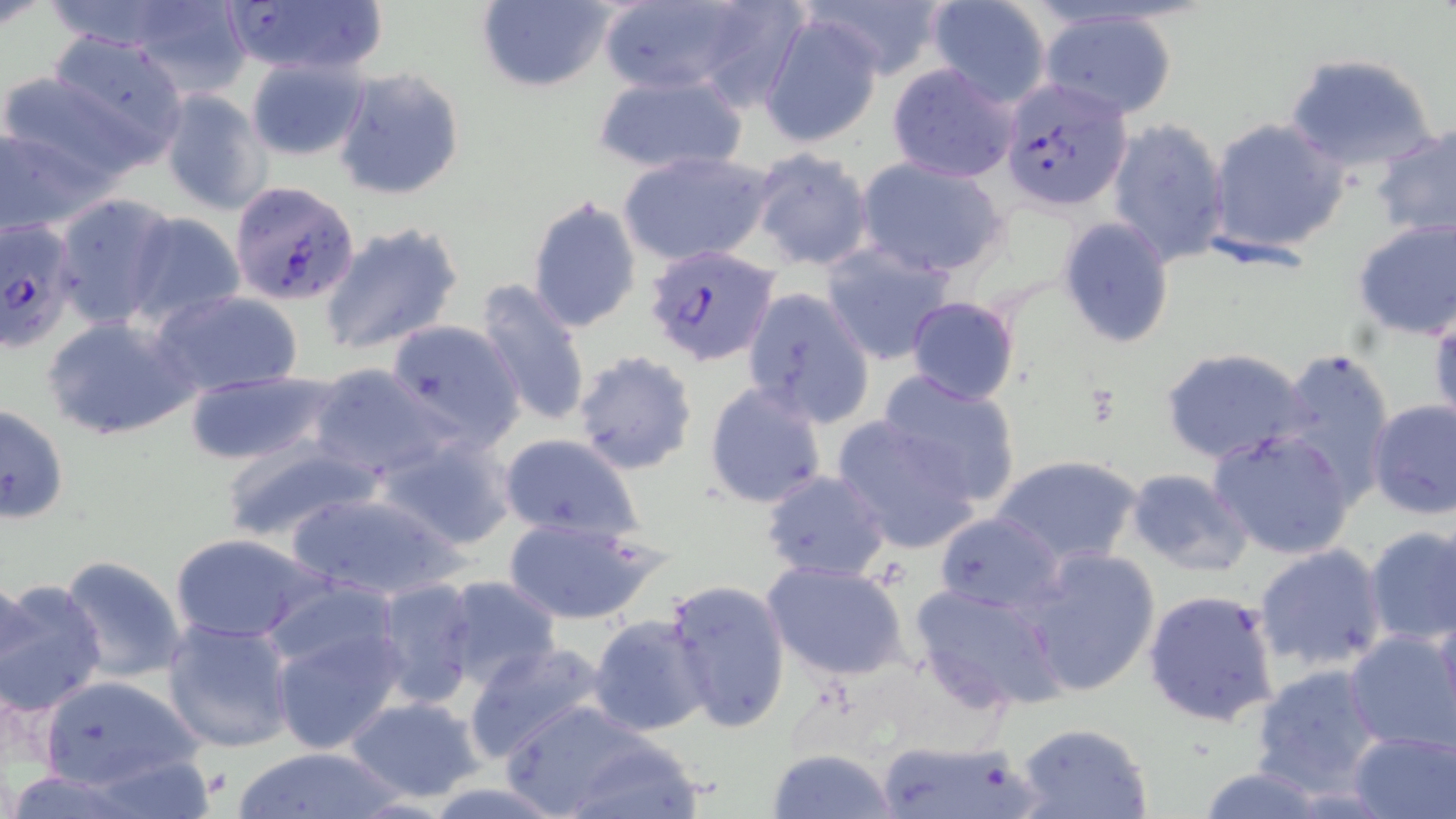

slide-level diagnosis = Plasmodium falciparum
modality = light microscopy
uninfected red blood cell locations = approximate bounding boxes as [x1, y1, x2, y2] in pixels: [801, 0, 950, 81], [221, 1, 383, 78], [472, 1, 615, 93], [590, 2, 765, 101], [925, 2, 1052, 108], [124, 3, 257, 99], [1040, 10, 1178, 120], [762, 13, 883, 148], [40, 31, 192, 162], [1282, 53, 1439, 175], [245, 56, 370, 160], [884, 61, 1021, 183], [0, 66, 151, 190], [332, 69, 465, 201], [591, 72, 748, 174], [158, 89, 273, 216], [1206, 117, 1351, 256], [1106, 118, 1231, 266], [0, 120, 106, 237], [1371, 121, 1456, 240], [618, 150, 774, 267], [749, 150, 874, 272], [856, 158, 1009, 278], [51, 193, 176, 329], [527, 197, 643, 335], [123, 212, 248, 327], [1058, 218, 1176, 349], [1352, 218, 1456, 340], [319, 222, 464, 356], [821, 243, 957, 366], [473, 278, 591, 430], [151, 289, 305, 398], [740, 289, 875, 428], [905, 296, 1021, 405], [1428, 302, 1456, 429], [41, 313, 200, 442], [386, 320, 523, 446], [1160, 345, 1312, 466], [1275, 348, 1393, 500], [571, 351, 698, 475], [308, 364, 452, 480], [181, 370, 342, 467], [878, 371, 1023, 507], [703, 380, 827, 510], [1367, 398, 1455, 519], [0, 404, 69, 525], [834, 414, 982, 555], [1207, 428, 1359, 561], [378, 432, 519, 551], [497, 435, 643, 545], [216, 439, 385, 543], [993, 454, 1142, 567], [1124, 468, 1254, 577], [759, 470, 892, 583], [280, 489, 468, 603], [934, 511, 1064, 616], [502, 514, 664, 625], [1361, 526, 1456, 648], [169, 531, 323, 644], [1253, 544, 1388, 672], [1018, 547, 1163, 696], [57, 555, 191, 685], [762, 560, 913, 681], [1, 574, 38, 695], [438, 575, 563, 690], [661, 577, 791, 736], [371, 578, 478, 708], [0, 579, 109, 717], [910, 582, 1068, 713], [1141, 588, 1282, 728], [269, 615, 409, 754], [587, 616, 712, 737], [162, 618, 298, 754], [1343, 630, 1456, 753], [463, 642, 608, 763], [1250, 662, 1388, 797], [37, 674, 206, 793], [343, 696, 488, 803], [502, 700, 683, 817], [1012, 721, 1155, 819], [1349, 728, 1455, 818], [555, 735, 710, 818], [873, 736, 1042, 819], [227, 747, 406, 818], [766, 748, 897, 819], [1189, 767, 1333, 819]
magnification = 1000x
stain = May-Grünwald-Giemsa
field of view = single
preparation = thin blood film
image size = 1456×819 pixels
Plasmodium falciparum-infected red blood cell locations = approximate bounding boxes as [x1, y1, x2, y2] in pixels: [998, 78, 1133, 212], [230, 180, 366, 308], [0, 215, 81, 352], [645, 246, 780, 366]